Report the malaria status of this cell.
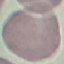
It is uninfected.

Giemsa stain. Acquired by smartphone through the microscope eyepiece. Cell patch, automatically extracted from a larger field of view and resized to 64 × 64 pixels. Thin blood smear.